State which parasite is depicted.
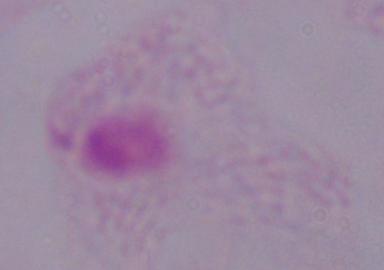

This is a trichomonad.

Captured at 1000x magnification. Micrograph.